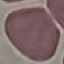 Result: no malaria parasites seen. Cell patch, automatically extracted from a larger field of view and resized to 64 × 64 pixels. Acquired by smartphone through the microscope eyepiece. Thin blood film. Giemsa stain.